Identify the parasite.
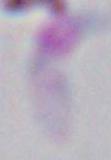
This is Toxoplasma gondii.

magnification: 1000x
modality: photomicrograph